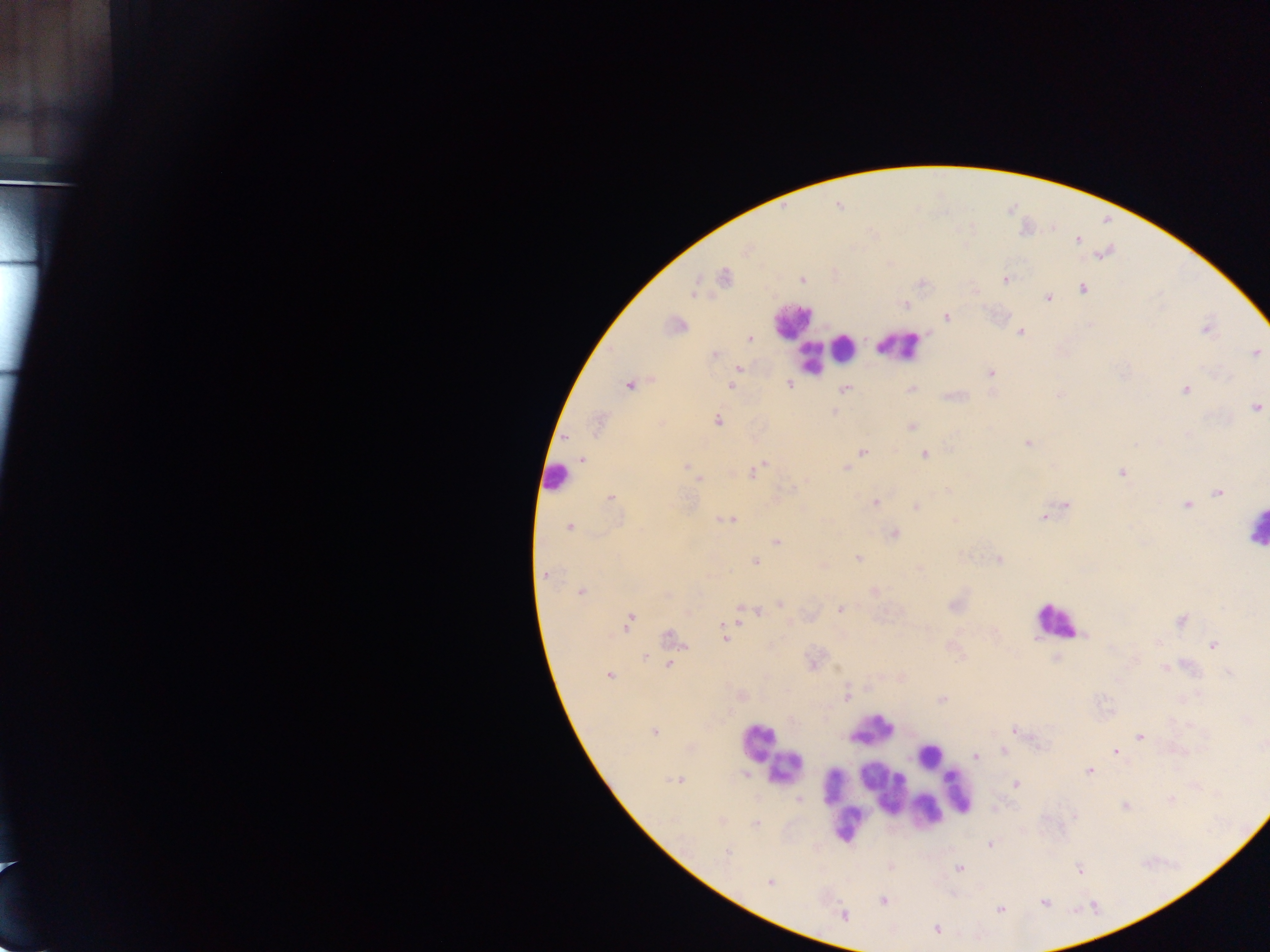
Approximate centers as {x, y} in pixels.
Summary:
  - Malaria parasite locations: {802, 281}, {1006, 282}, {1081, 289}, {1048, 297}, {947, 316}, {680, 324}, {1020, 331}, {749, 338}, {714, 354}, {1257, 354}, {740, 369}, {990, 372}, {789, 385}, {629, 386}, {733, 386}, {846, 388}, {912, 389}, {1185, 390}, {950, 395}, {1256, 408}, {834, 410}, {719, 420}, {597, 425}, {911, 425}, {567, 438}, {1027, 442}, {925, 455}, {857, 456}, {582, 460}, {766, 464}, {686, 465}, {845, 468}, {756, 470}, {1121, 471}, {750, 472}, {699, 480}, {795, 487}, {947, 491}, {1218, 494}, {609, 497}, {875, 502}, {1066, 503}, {1185, 504}, {916, 506}, {1042, 517}, {716, 519}, {733, 519}, {957, 519}, {723, 520}, {567, 527}, {894, 533}, {778, 542}, {964, 555}, {859, 559}, {1000, 560}, {755, 562}, {918, 568}, {545, 574}, {583, 591}, {874, 592}, {780, 605}, {740, 607}, {952, 607}, {839, 609}, {629, 618}, {750, 618}, {1181, 621}, {627, 629}, {669, 638}, {724, 640}, {1212, 645}, {645, 657}, {669, 664}, {836, 667}, {1166, 668}, {1228, 672}, {609, 676}, {846, 696}, {941, 699}, {1185, 699}, {1011, 729}, {1140, 737}, {1116, 750}, {975, 756}, {1088, 770}, {745, 775}, {1015, 783}, {798, 800}, {1170, 800}, {1125, 807}, {755, 822}, {727, 852}, {959, 869}, {1079, 869}, {770, 884}, {1044, 902}, {999, 910}, {936, 929}
  - Leukocyte locations: {783, 321}, {901, 342}, {847, 343}, {808, 361}, {552, 481}, {1252, 533}, {1058, 628}, {877, 729}, {758, 737}, {928, 755}, {781, 774}, {837, 785}, {883, 788}, {958, 789}, {926, 812}, {846, 834}
  - Field of view: single
  - Image size: 1270×952 pixels
  - Country: Ghana
  - Capture: mobile-phone photograph through a microscope
  - Preparation: thick blood film